Describe the morphology of the red blood cells.
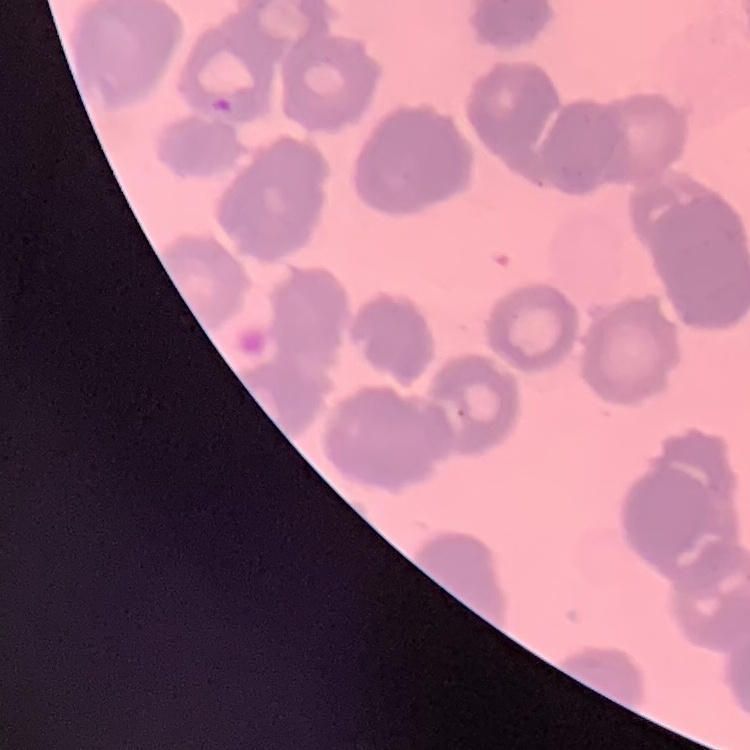
Rouleaux formation.

{
  "stain": "Field's or Giemsa",
  "image_type": "one tile cut from a larger photomicrograph",
  "preparation": "thin blood smear"
}